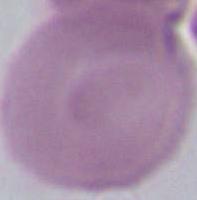
identification = erythrocyte
modality = micrograph
magnification = 1000x